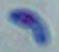 Toxoplasma gondii is shown. 1000x magnification. Micrograph.